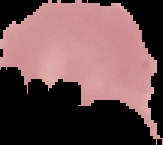
Summary:
  - Preparation: thin blood film
  - Image type: segmented cell region with the area outside set to black
  - Image size: 163×145 pixels
  - Result: malaria parasites detected